Name the blood parasite species.
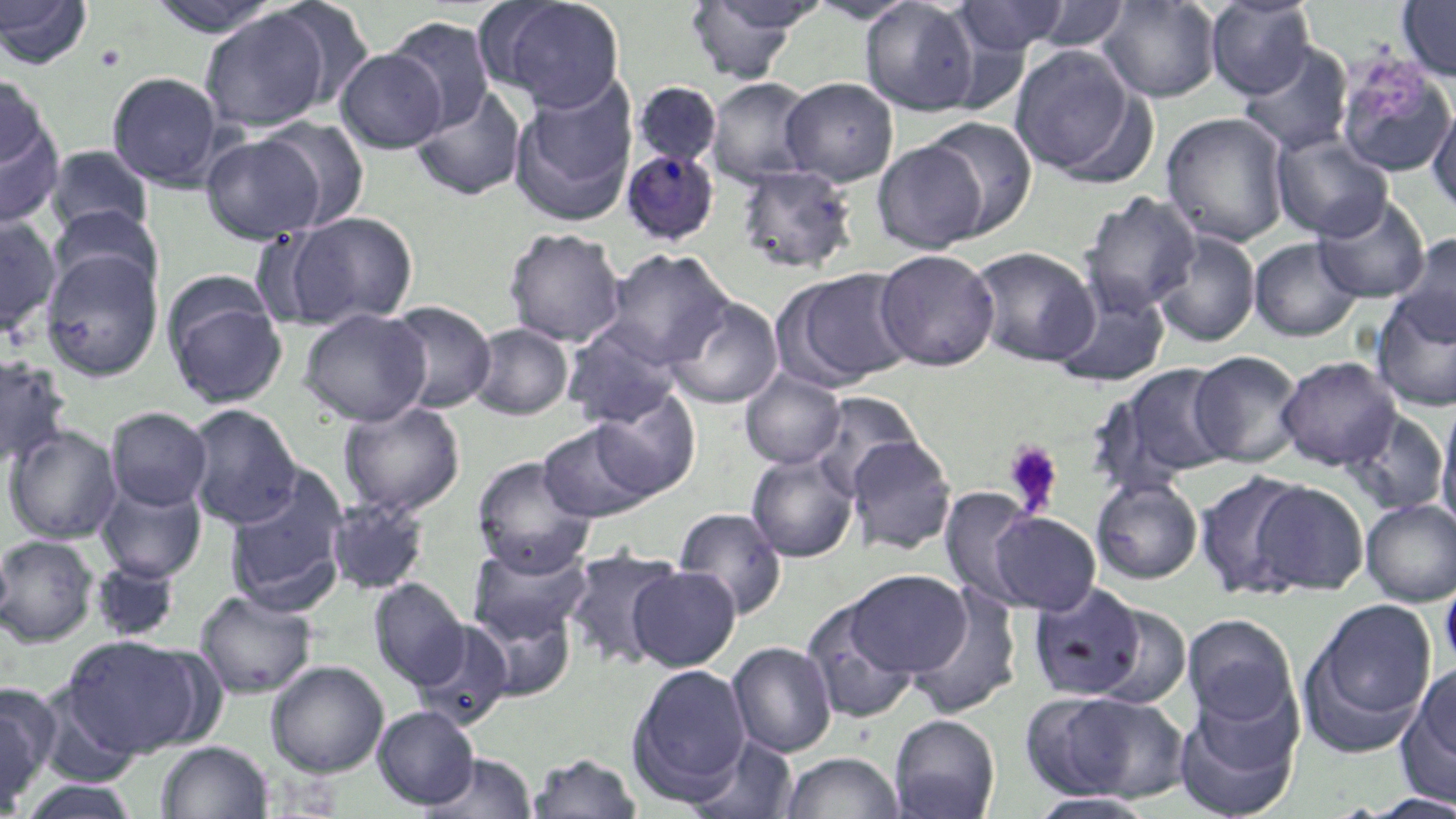
Plasmodium malariae.

Summary:
  - Coordinate format: approximate bounding boxes as (x1,y1)-(x2,y2) corner pairs in pixels
  - Platelet locations: (93,44)-(127,73), (1002,440)-(1063,516)
  - Plasmodium malariae-infected red blood cell locations: (620,149)-(721,247)
  - Uninfected red blood cell locations: (0,0)-(94,69), (264,0)-(377,112), (482,0)-(627,112), (859,0)-(981,115), (1204,0)-(1316,99), (1396,0)-(1456,81), (146,1)-(287,37), (683,1)-(811,84), (804,1)-(921,24), (951,1)-(1069,57), (1097,1)-(1221,102), (1022,2)-(1134,54), (199,8)-(335,133), (384,17)-(497,131), (1238,42)-(1354,156), (1008,44)-(1143,179), (335,48)-(448,153), (1332,53)-(1455,177), (107,71)-(226,189), (0,75)-(52,171), (706,76)-(818,187), (780,77)-(898,186), (509,80)-(638,225), (632,81)-(722,167), (410,86)-(527,201), (1427,97)-(1456,217), (1160,113)-(1290,246), (0,116)-(64,230), (922,116)-(1038,238), (255,117)-(371,230), (200,132)-(328,243), (1272,132)-(1393,241), (872,140)-(987,253), (45,145)-(154,239), (736,165)-(858,275), (1078,190)-(1202,315), (1314,195)-(1430,303), (49,205)-(159,296), (283,212)-(419,327), (0,216)-(62,335), (503,227)-(627,346), (1152,230)-(1260,347), (1393,234)-(1456,345), (1250,238)-(1362,341), (969,246)-(1099,367), (40,249)-(163,381), (603,249)-(733,367), (874,249)-(999,371), (776,267)-(914,390), (164,285)-(288,409), (1052,286)-(1170,387), (1369,291)-(1456,411), (664,296)-(783,408), (385,300)-(497,413), (299,308)-(431,426), (468,322)-(573,420), (562,322)-(683,429), (1189,350)-(1305,468), (0,351)-(72,470), (1276,355)-(1402,471), (1107,363)-(1236,487), (740,370)-(846,469), (588,389)-(702,500), (808,392)-(925,498), (1435,399)-(1456,534), (338,400)-(466,516), (183,404)-(303,528), (105,406)-(212,511), (1343,409)-(1449,515), (537,420)-(660,523), (3,425)-(122,544), (847,435)-(957,555), (745,452)-(859,562), (471,455)-(597,576), (223,466)-(351,614), (1193,470)-(1316,599), (1091,477)-(1203,584), (96,479)-(207,582), (1247,480)-(1370,596), (938,487)-(1042,607), (325,495)-(432,596), (1360,499)-(1456,606), (672,507)-(789,619), (986,511)-(1101,615), (0,534)-(99,647), (469,541)-(593,646), (562,547)-(685,669), (90,558)-(181,642), (627,565)-(742,671), (844,569)-(973,677), (1440,570)-(1456,675), (369,579)-(469,688), (1027,583)-(1149,701), (907,587)-(1023,719), (194,590)-(318,699), (801,596)-(922,726), (1300,599)-(1437,754), (1085,602)-(1193,710), (471,603)-(578,702), (1182,614)-(1298,728), (409,619)-(515,731), (58,634)-(215,758), (727,641)-(837,757), (265,660)-(389,777), (1401,660)-(1456,799), (626,663)-(752,803), (0,683)-(59,811), (1174,686)-(1304,819), (1052,693)-(1193,802), (373,705)-(479,809), (888,714)-(1000,819), (689,735)-(799,819), (156,741)-(273,819), (779,751)-(904,819), (422,753)-(538,818), (528,753)-(643,818), (17,778)-(141,818), (1360,792)-(1456,818), (1028,793)-(1157,818)
  - Image size: 1456×819 pixels
  - Preparation: thin blood film
  - Modality: optical microscopy
  - Stain: May-Grünwald-Giemsa
  - Magnification: 1000x
  - Field of view: single